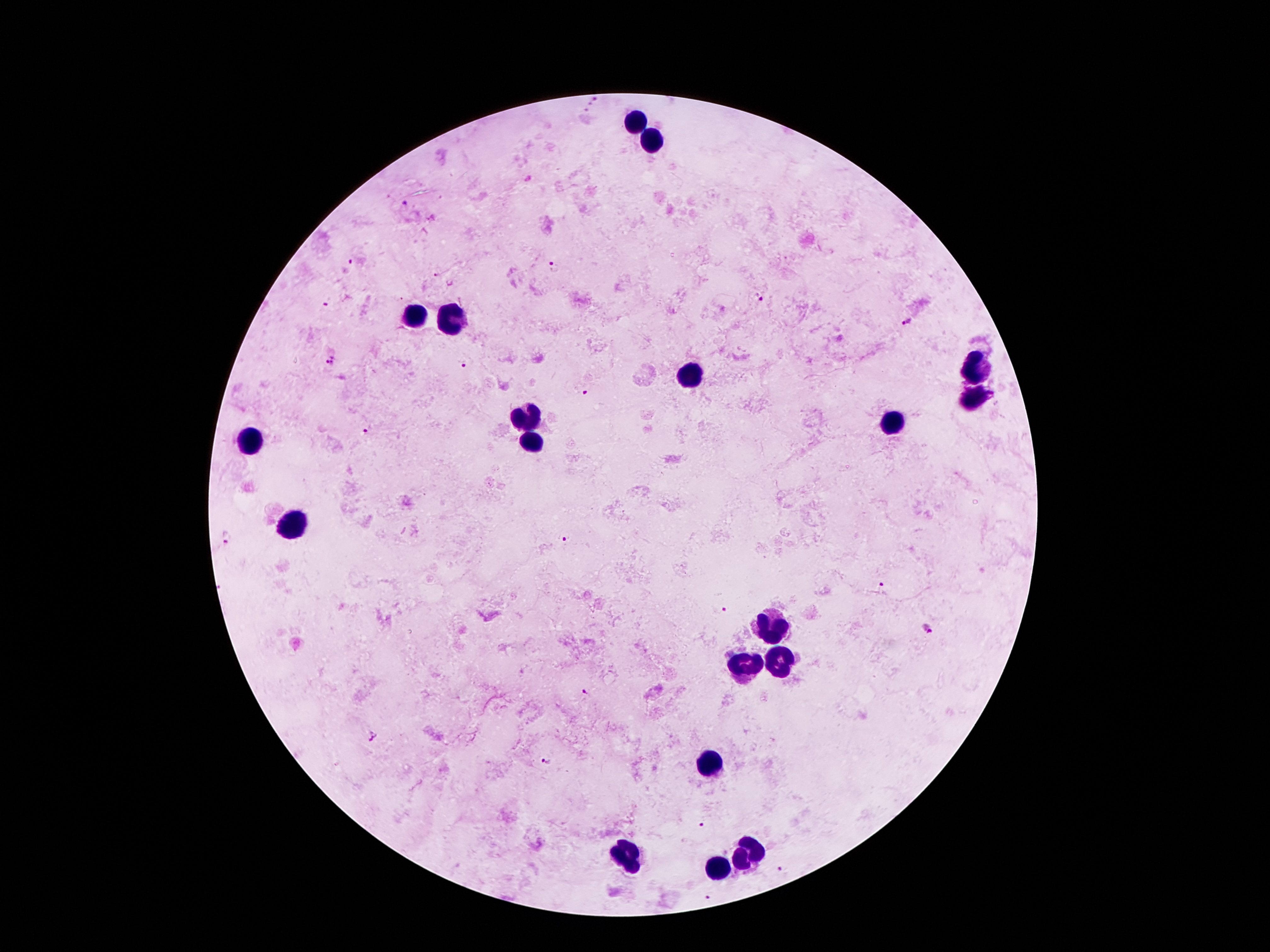

Approximate centers as [x, y] in pixels.
Summary:
  - Malaria parasite locations: [594, 100], [404, 201], [352, 261], [553, 267], [760, 298], [327, 302], [907, 322], [332, 361], [463, 363], [584, 391], [364, 430], [227, 537], [564, 537], [882, 584], [725, 608], [928, 628], [586, 692], [374, 736], [547, 760], [700, 825], [782, 867], [709, 897]
  - Leukocyte locations: [631, 120], [651, 141], [447, 313], [410, 314], [978, 372], [692, 375], [975, 400], [522, 416], [891, 427], [531, 439], [251, 441], [292, 525], [775, 625], [780, 662], [748, 666], [713, 762], [625, 857], [745, 857], [716, 869]
  - Magnification: 100x
  - Image size: 1270×952 pixels
  - Field of view: one from this slide
  - Preparation: thick blood smear
  - Stain: Giemsa
  - Patient malaria status: positive for Plasmodium falciparum
  - Capture: smartphone camera through the microscope eyepiece